Identify the cell.
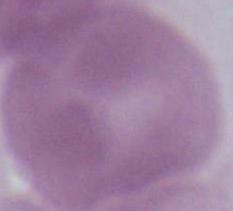

An erythrocyte.

Photomicrograph. Captured at 1000x magnification.